Classify this cell by malaria status.
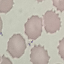

Uninfected.

image type = cell patch, automatically extracted from a larger field of view and resized to 64 × 64 pixels
stain = Giemsa
capture = smartphone through the microscope eyepiece
preparation = thin smear